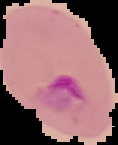

Summary:
  - Image type: segmented cell region on a black background
  - Malaria status: parasitized
  - Preparation: thin blood film
  - Image size: 118×145 pixels